Classify this cell by malaria status.
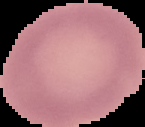

Uninfected.

Summary:
  - Image type: segmented cell region with the area outside set to black
  - Image size: 145×127 pixels
  - Preparation: thin blood film